State which parasite is depicted.
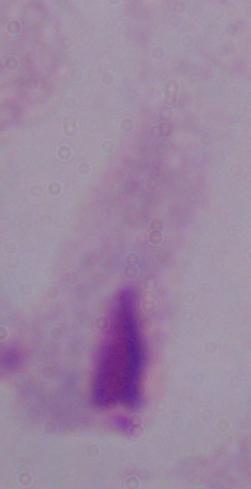

A trichomonad.

Summary:
  - Modality: micrograph
  - Magnification: 1000x